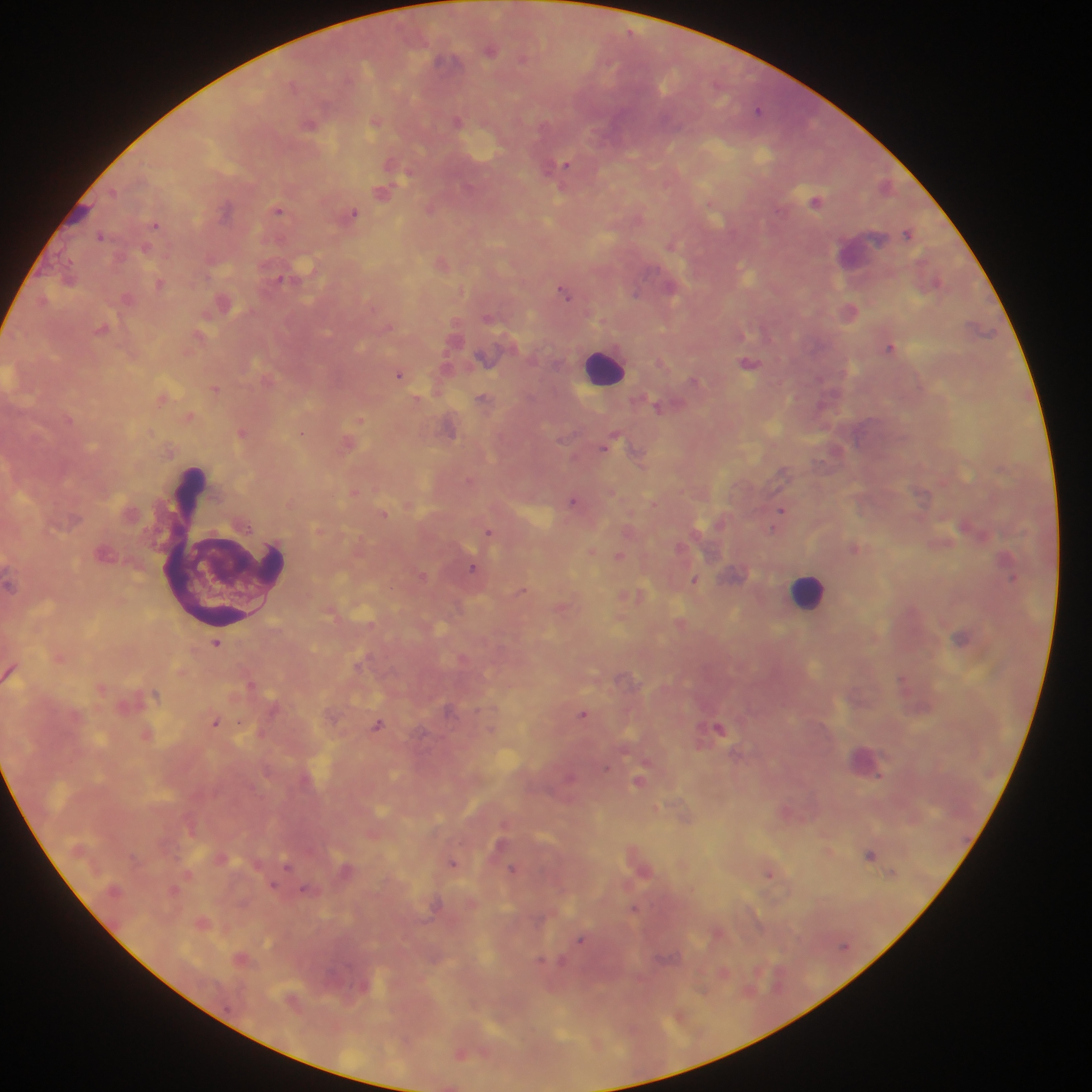

Approximate centers as x y in pixels.
Summary:
  - Leukocyte locations (subset; some below the resolvable size): 865 254; 603 366; 224 549; 808 590
  - Plasmodium parasite locations: 491 50; 523 58; 442 60; 758 110; 457 121; 375 122; 310 124; 565 165; 405 175; 381 192; 817 201; 430 208; 226 209; 278 210; 353 214; 156 225; 907 234; 101 235; 671 245; 146 249; 281 278; 936 281; 160 284; 670 288; 636 292; 564 293; 892 348; 749 363; 399 374; 694 380; 216 388; 483 397; 658 406; 360 419; 302 433; 613 436; 609 443; 638 458; 784 473; 572 501; 781 511; 777 520; 773 530; 488 531; 854 547; 619 556; 472 568; 1012 577; 695 579; 522 590; 962 638; 216 643; 357 664; 902 679; 251 684; 155 693; 583 713; 215 722; 378 725; 719 728; 871 767; 638 781; 870 855; 453 863; 287 866; 513 868; 770 874; 274 886; 305 889; 634 909; 581 940; 541 960
  - Image size: 1092×1092 pixels
  - Capture: mobile-phone photograph through a microscope
  - Country: Ghana
  - Field of view: single
  - Preparation: thick blood smear